Outline each uninfected red blood cell.
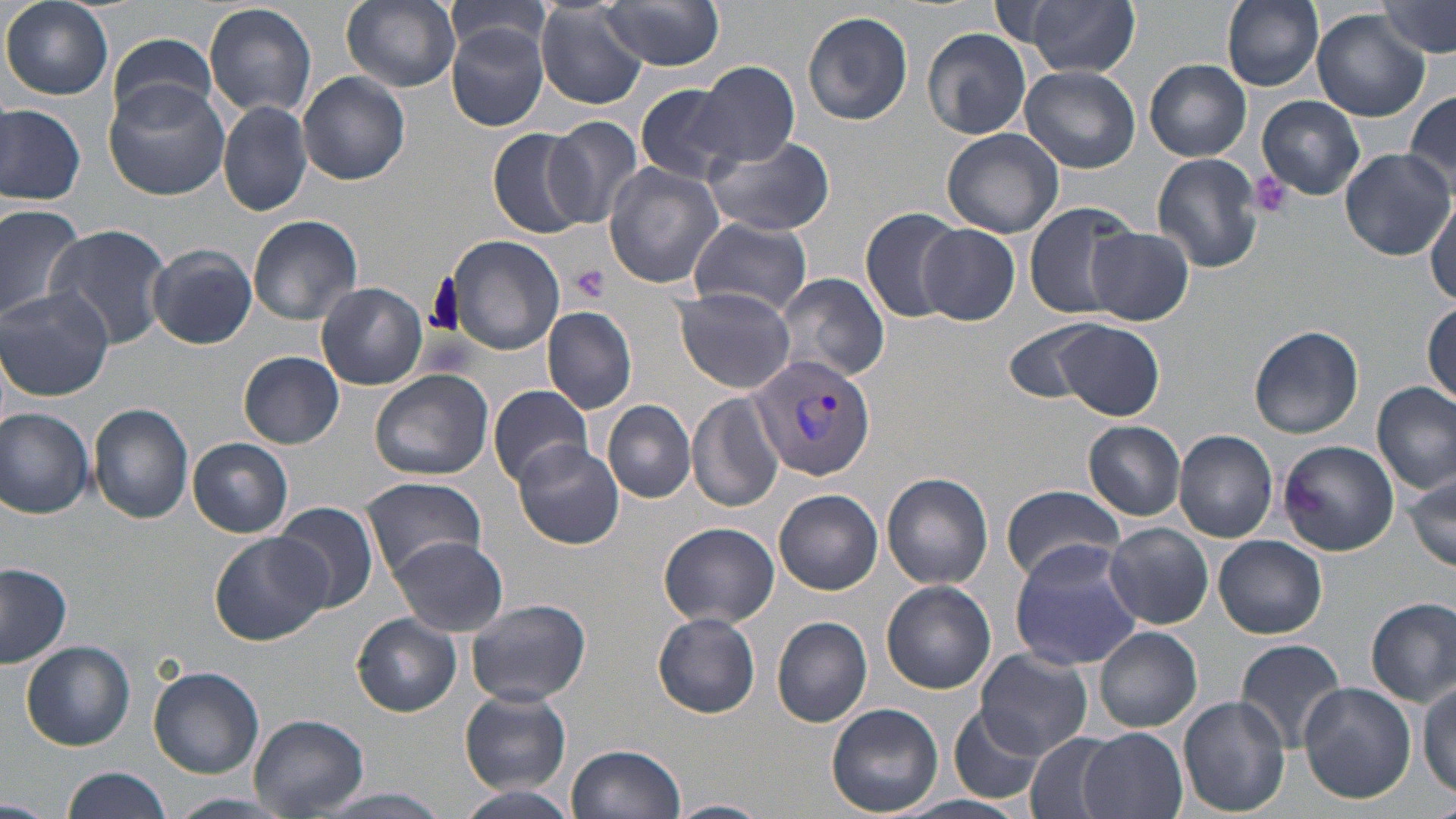
Approximate bounding boxes as (x1, y1, x2, y2) in pixels.
Uninfected red blood cells: (339, 0, 463, 94), (445, 0, 557, 70), (1219, 0, 1326, 93), (533, 1, 650, 109), (2, 2, 113, 100), (204, 2, 317, 117), (598, 2, 726, 70), (1380, 3, 1453, 63), (1021, 4, 1139, 78), (803, 10, 914, 125), (1312, 12, 1430, 121), (446, 22, 550, 131), (922, 28, 1031, 139), (106, 38, 219, 130), (1145, 59, 1251, 161), (693, 62, 800, 168), (1020, 66, 1139, 172), (298, 70, 410, 184), (103, 81, 230, 200), (635, 82, 744, 185), (1405, 88, 1456, 189), (1257, 94, 1366, 200), (216, 100, 311, 216), (0, 102, 86, 205), (542, 114, 645, 229), (941, 127, 1065, 238), (486, 128, 591, 238), (701, 134, 835, 237), (1338, 147, 1454, 261), (1152, 153, 1267, 273), (602, 162, 725, 288), (1427, 196, 1456, 305), (0, 201, 86, 327), (1022, 203, 1138, 320), (859, 208, 961, 321), (246, 214, 363, 325), (688, 216, 811, 315), (44, 223, 173, 351), (917, 223, 1022, 325), (1085, 226, 1193, 326), (442, 233, 567, 356), (146, 245, 257, 349), (775, 271, 888, 383), (317, 283, 428, 389), (673, 287, 797, 395), (1, 289, 114, 401), (1423, 301, 1455, 409), (542, 305, 637, 414), (1047, 320, 1167, 421), (1006, 321, 1112, 405), (1249, 325, 1364, 438), (237, 351, 345, 448), (369, 368, 494, 480), (1372, 382, 1455, 493), (489, 385, 593, 487), (688, 392, 786, 514), (603, 400, 696, 503), (89, 402, 193, 524), (0, 407, 94, 521), (1083, 420, 1186, 522), (1173, 429, 1278, 544), (188, 438, 293, 538), (513, 438, 624, 549), (1278, 439, 1398, 556), (1406, 470, 1456, 572), (883, 473, 993, 589), (360, 476, 488, 576), (1000, 483, 1126, 583), (775, 490, 882, 595), (272, 501, 380, 612), (659, 522, 780, 631), (1104, 523, 1212, 629), (210, 532, 332, 646), (387, 535, 509, 636), (1213, 535, 1327, 639), (1009, 541, 1143, 671), (0, 563, 73, 667), (882, 580, 996, 693), (1367, 597, 1455, 705), (466, 598, 591, 707), (654, 612, 760, 718), (352, 613, 462, 716), (772, 616, 874, 728), (1095, 626, 1202, 733), (1234, 637, 1346, 750), (21, 641, 135, 749), (973, 650, 1093, 758), (149, 666, 265, 778), (1417, 677, 1455, 799), (1298, 681, 1416, 804), (459, 689, 575, 794), (1177, 696, 1290, 817), (828, 703, 943, 817), (948, 707, 1042, 805), (249, 713, 367, 818), (1079, 727, 1189, 819), (1025, 732, 1126, 819), (567, 744, 685, 819), (61, 766, 175, 819), (455, 787, 582, 818), (167, 793, 292, 817), (0, 797, 49, 816), (664, 800, 771, 819).

slide_level_diagnosis: Plasmodium vivax
magnification: 1000x
image_size: 1456×819 pixels
field_of_view: single
platelet_locations: 'approximate bounding boxes as (x1, y1, x2, y2) in pixels: (1249, 172, 1293, 218), (569, 263, 610, 303)'
preparation: thin blood smear
plasmodium_vivax_infected_red_blood_cell_locations: 'approximate bounding boxes as (x1, y1, x2, y2) in pixels: (752, 356, 877, 481)'
stain: May-Grünwald-Giemsa
modality: light microscopy